Classify this cell by malaria status.
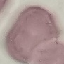

It is uninfected.

image type = automatically extracted cell patch, resized to 64 × 64 pixels
preparation = thin blood smear
capture = smartphone camera at the microscope eyepiece
stain = Giemsa